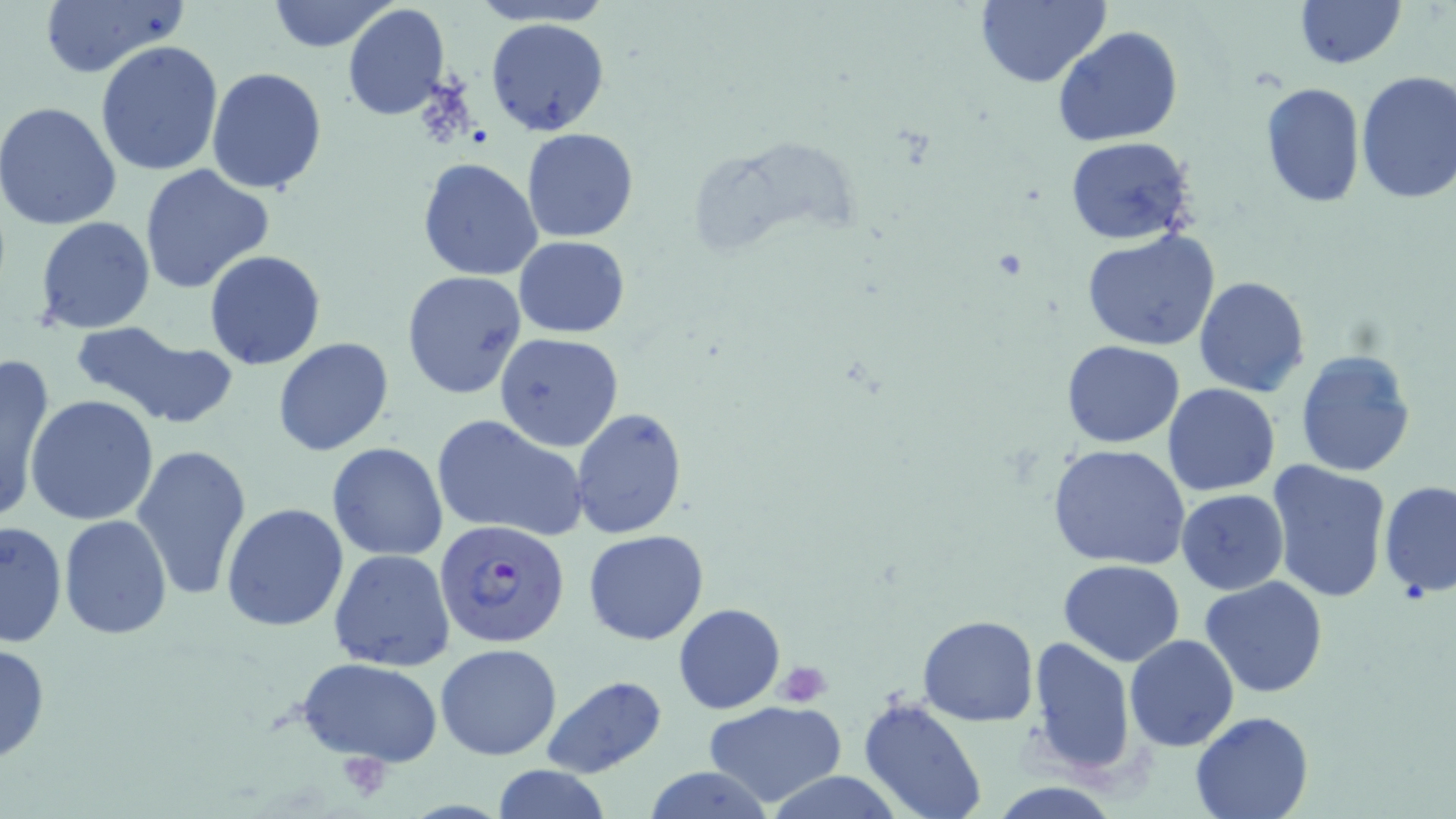

Summary:
  - Coordinate format: approximate bounding boxes as (x1,y1)-(x2,y2) corner pairs in pixels
  - Plasmodium falciparum-infected red blood cell locations: (435,518)-(570,649)
  - Platelet locations: (776,661)-(832,707), (336,751)-(394,801)
  - Uninfected red blood cell locations: (37,0)-(190,79), (265,0)-(400,53), (464,0)-(618,26), (974,0)-(1111,88), (1296,0)-(1404,69), (342,4)-(450,122), (484,17)-(612,138), (1053,26)-(1183,148), (94,40)-(224,178), (206,66)-(328,195), (1354,71)-(1456,203), (1260,82)-(1366,210), (0,101)-(121,231), (520,129)-(638,243), (1064,135)-(1197,246), (417,158)-(544,280), (139,162)-(276,294), (34,216)-(157,334), (1081,228)-(1222,352), (514,236)-(631,338), (204,250)-(327,371), (400,270)-(527,399), (1193,276)-(1310,396), (68,321)-(234,429), (495,333)-(625,452), (273,338)-(394,456), (1061,341)-(1186,448), (1295,348)-(1418,478), (0,355)-(55,525), (1162,383)-(1282,497), (27,395)-(159,526), (570,408)-(687,538), (432,412)-(588,542), (132,443)-(253,599), (327,443)-(449,562), (1047,443)-(1191,571), (1265,458)-(1393,602), (1378,480)-(1456,598), (1176,490)-(1289,594), (221,503)-(349,633), (59,516)-(172,640), (1,519)-(66,649), (583,529)-(709,645), (329,548)-(456,671), (1058,560)-(1186,666), (1201,575)-(1328,697), (674,603)-(786,714), (918,614)-(1038,726), (1026,635)-(1139,777), (1125,635)-(1239,751), (0,641)-(52,765), (435,643)-(562,761), (298,658)-(443,765), (540,675)-(666,779), (858,697)-(987,819), (703,700)-(848,806), (1190,711)-(1312,819), (490,765)-(613,819), (642,765)-(776,819), (758,769)-(907,819)
  - Slide-level diagnosis: Plasmodium falciparum
  - Field of view: one of a larger specimen
  - Stain: May-Grünwald-Giemsa
  - Magnification: 1000x
  - Modality: light microscopy
  - Preparation: thin blood film
  - Image size: 1456×819 pixels